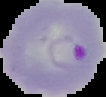 Result: Plasmodium parasites identified. From a thin blood smear. Image is 106×97 pixels. Segmented cell region on a black background.